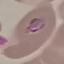

malaria_status: parasitized
image_type: automatically extracted cell patch, resized to 64 × 64 pixels
capture: smartphone through the microscope eyepiece
stain: Giemsa
preparation: thin blood film